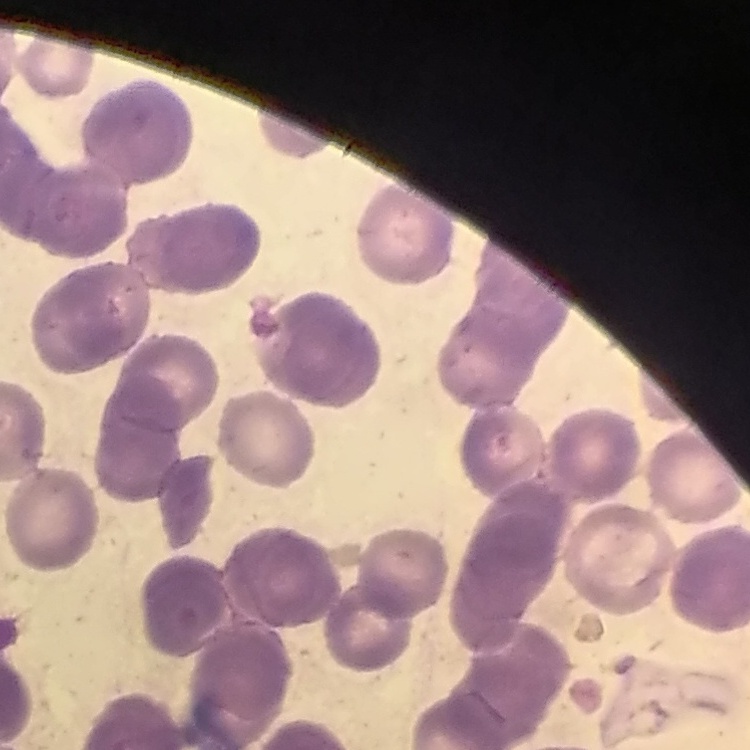
{
  "erythrocyte_morphology": "rouleaux formation",
  "image_type": "square crop of a larger photomicrograph",
  "stain": "Field's or Giemsa",
  "preparation": "thin blood smear"
}